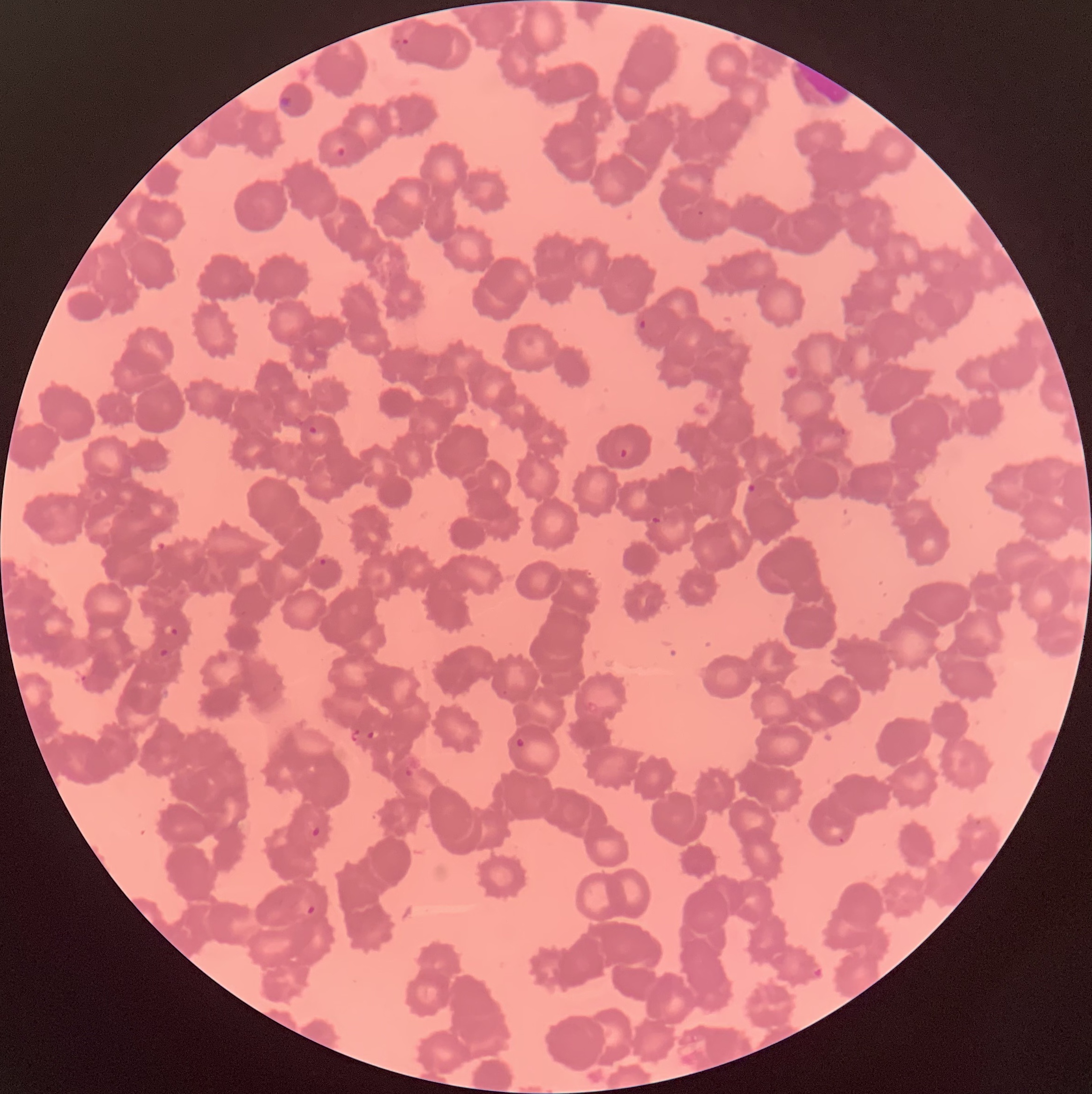
{
  "preparation": "thin blood film",
  "red_blood_cell_morphology": "rouleaux formation",
  "modality": "optical microscopy",
  "image_size": "1092×1094 pixels",
  "plasmodium_parasite_locations": "approximate bounding boxes as (x1, y1, x2, y2) in pixels: (389, 34, 412, 53), (335, 145, 348, 160), (636, 318, 649, 331), (307, 424, 319, 437), (618, 447, 629, 460), (746, 482, 757, 494), (650, 515, 661, 525), (317, 557, 328, 568), (164, 624, 179, 637), (158, 647, 170, 657), (347, 727, 362, 744), (366, 728, 380, 741), (514, 736, 527, 749), (402, 766, 414, 779), (310, 826, 321, 838), (305, 904, 317, 916), (810, 963, 826, 982)"
}